Report the malaria status of this cell.
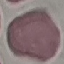
It is uninfected.

Summary:
  - Image type: automatically extracted cell patch, resized to 64 × 64 pixels
  - Capture: smartphone camera at the microscope eyepiece
  - Stain: Giemsa
  - Preparation: thin blood film